Give the position of every Plasmodium parasite.
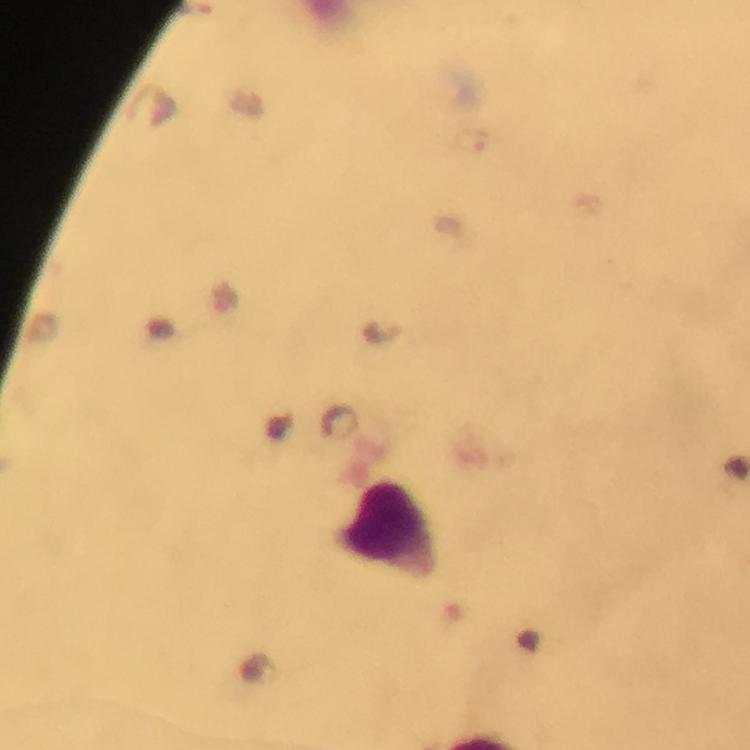
Approximate centers as {x, y} in pixels.
Plasmodium parasites: {471, 142}, {380, 331}.

leukocyte locations = approximate centers as {x, y} in pixels: {389, 526}
capture = smartphone camera through the microscope
magnification = 100x
preparation = thick blood smear
cropped from = a single field of view
stain = Giemsa
image size = 750×750 pixels
immersion oil = applied
context = from a diagnostic examination for malaria